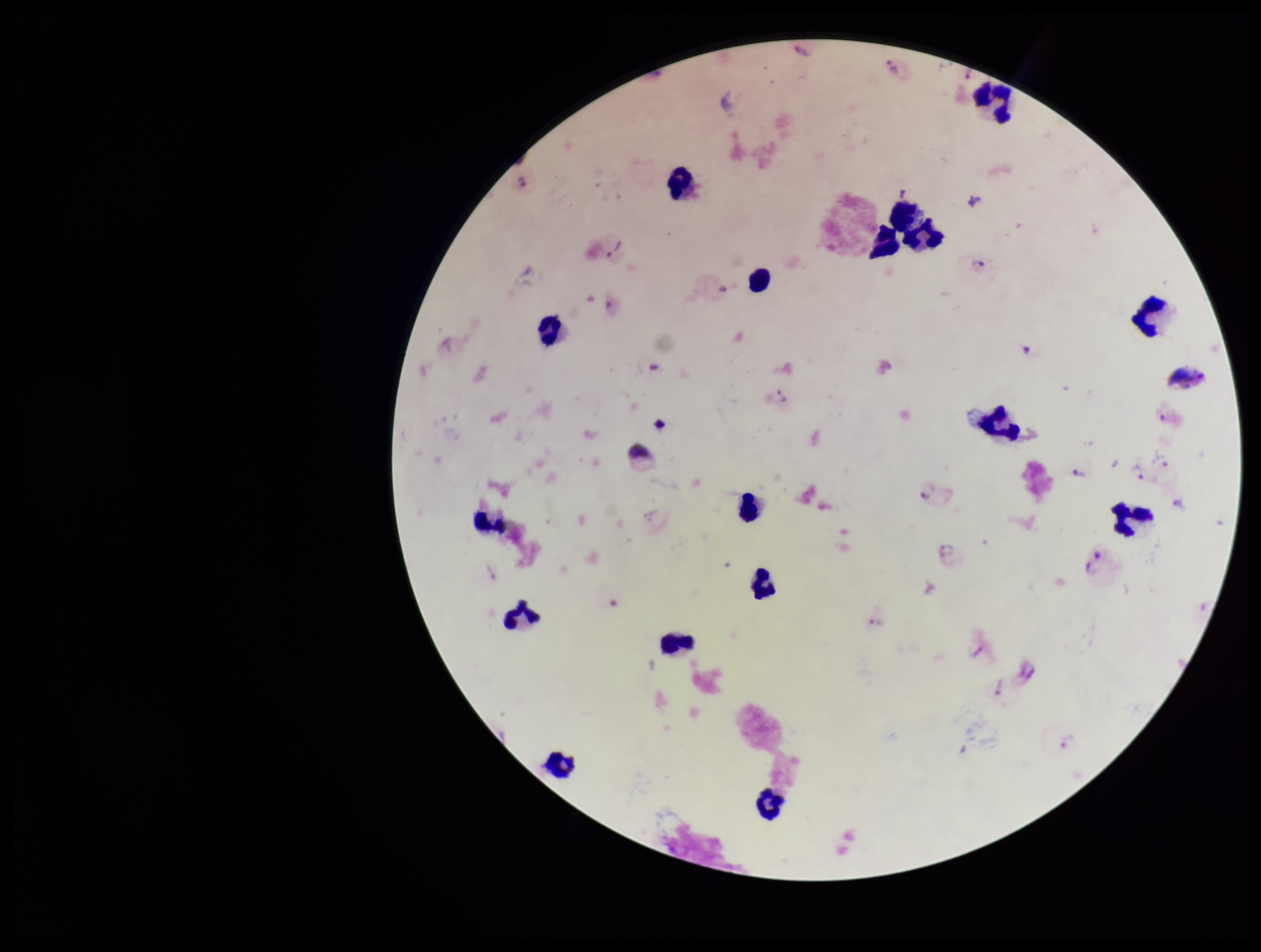 Patient malaria status: infected. Plasmodium parasites: seen. Parasite count: 19. Photographed through the microscope eyepiece with a smartphone camera. Preparation: thick. Species reported for this patient: Plasmodium vivax. Stained with Giemsa. One field from this slide. Image is 1261×952 pixels. Leukocyte count: 17.